Outline each uninfected red blood cell.
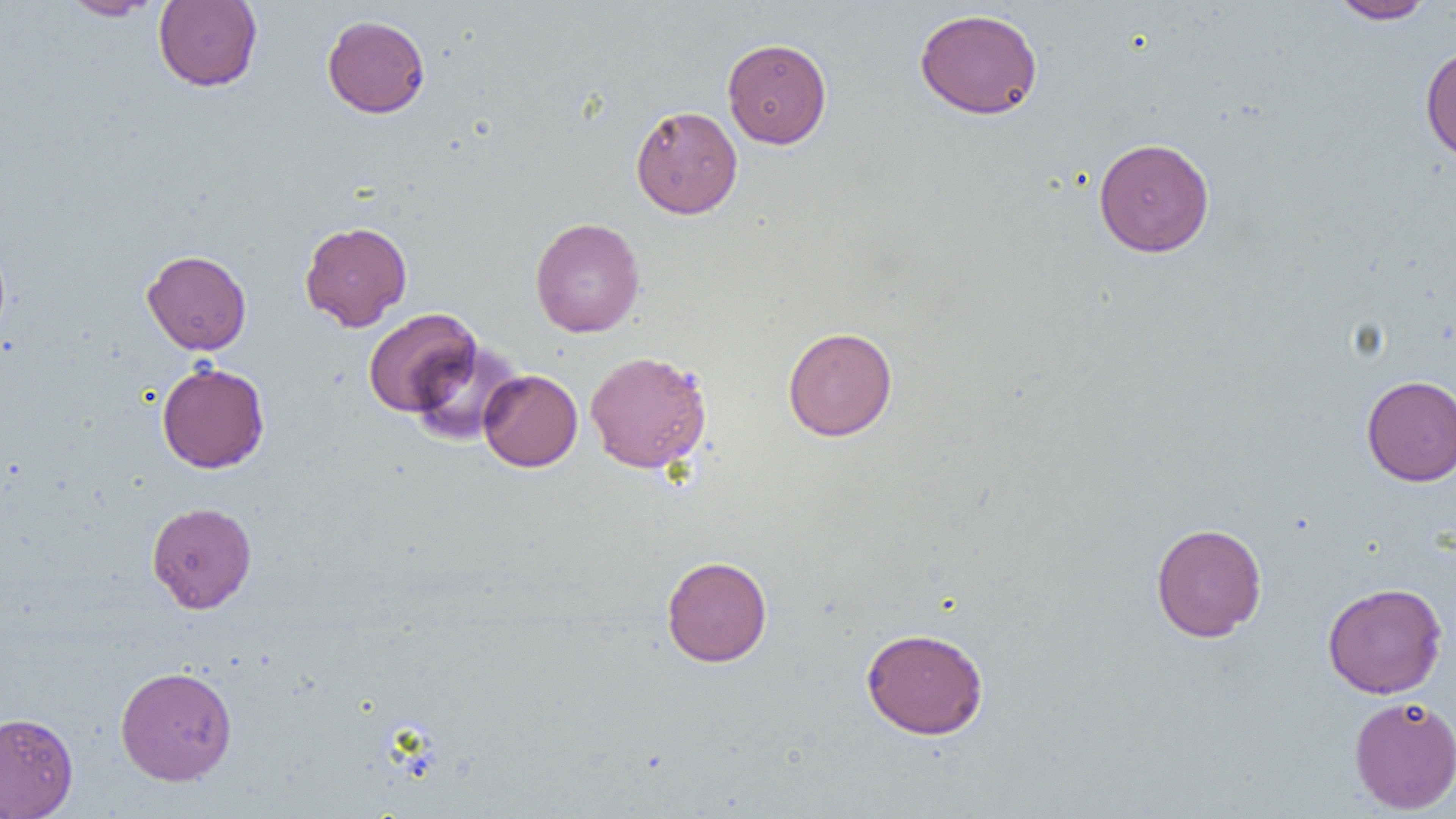

Approximate bounding boxes as named x1/y1/x2/y2 corners in pixels.
Uninfected red blood cells: (x1=153, y1=0, x2=262, y2=91), (x1=1329, y1=0, x2=1435, y2=24), (x1=60, y1=1, x2=160, y2=20), (x1=914, y1=8, x2=1043, y2=119), (x1=322, y1=15, x2=430, y2=118), (x1=722, y1=38, x2=832, y2=149), (x1=1420, y1=44, x2=1456, y2=164), (x1=630, y1=105, x2=743, y2=219), (x1=1093, y1=137, x2=1215, y2=257), (x1=530, y1=217, x2=645, y2=337), (x1=299, y1=221, x2=412, y2=331), (x1=0, y1=238, x2=11, y2=344), (x1=142, y1=250, x2=251, y2=355), (x1=363, y1=308, x2=481, y2=418), (x1=783, y1=326, x2=897, y2=441), (x1=408, y1=340, x2=525, y2=446), (x1=585, y1=350, x2=712, y2=473), (x1=156, y1=362, x2=269, y2=473), (x1=479, y1=369, x2=582, y2=472), (x1=1361, y1=375, x2=1456, y2=485), (x1=146, y1=501, x2=257, y2=613), (x1=1151, y1=522, x2=1267, y2=642), (x1=661, y1=555, x2=772, y2=667), (x1=1322, y1=582, x2=1448, y2=698), (x1=861, y1=627, x2=989, y2=739), (x1=115, y1=665, x2=237, y2=785), (x1=1349, y1=695, x2=1456, y2=814), (x1=0, y1=712, x2=78, y2=818).

Summary:
  - Slide-level diagnosis: negative for blood parasites
  - Image size: 1456×819 pixels
  - Field of view: single
  - Modality: light microscopy
  - Magnification: 1000x
  - Preparation: thin blood film